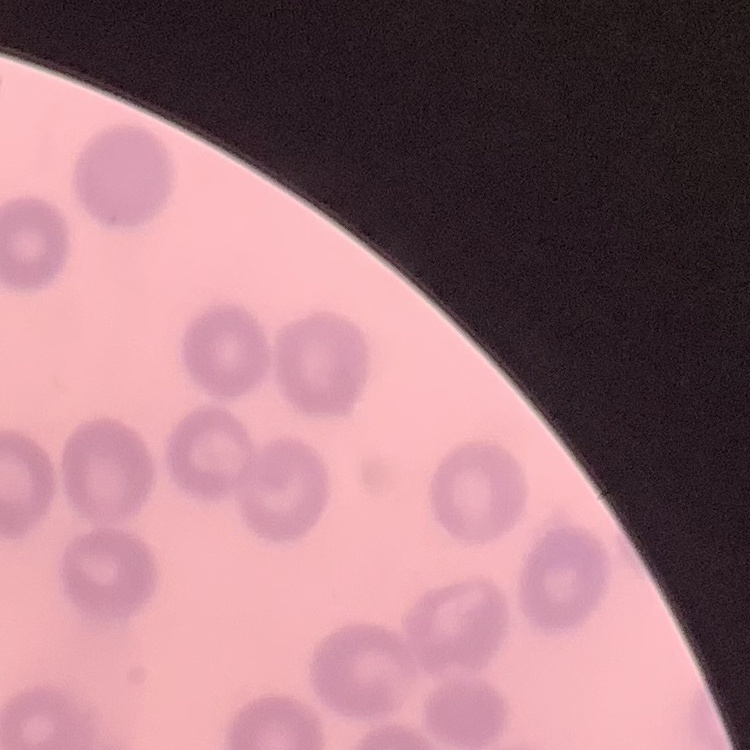

The erythrocytes exhibit no rouleaux formation. Thin peripheral smear. One tile cut from a larger photomicrograph. Stained with either Field's or Giemsa.